Comment on the morphology of the erythrocytes.
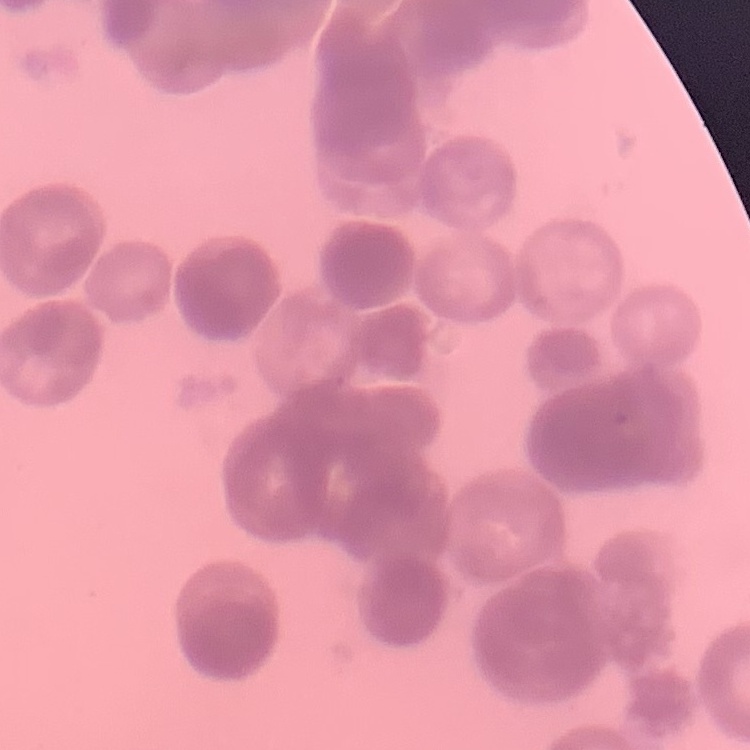

They show rouleaux formation.

Summary:
  - Preparation: thin blood smear
  - Stain: Field's or Giemsa
  - Image type: square crop of a larger photomicrograph